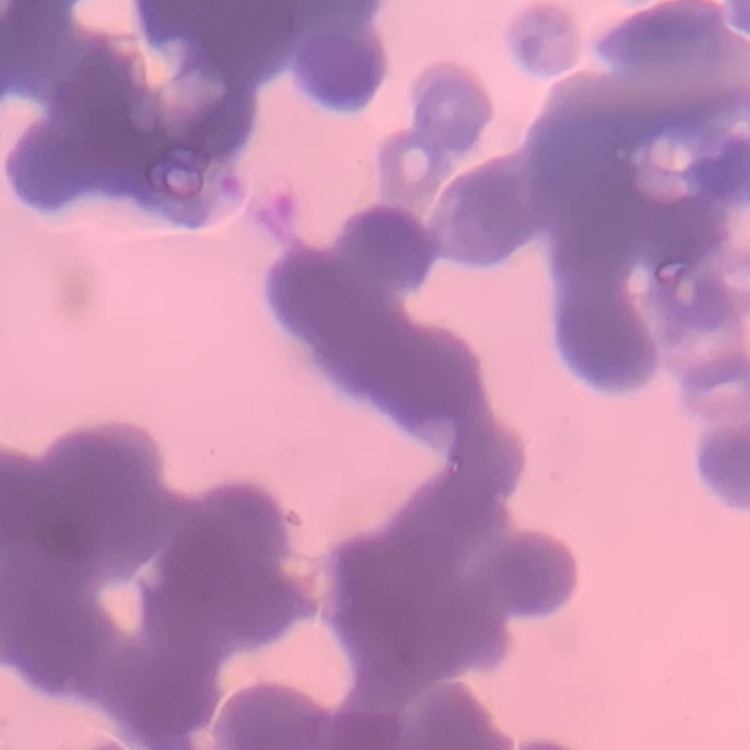
Summary:
  - Red blood cell morphology: rouleaux formation
  - Preparation: thin blood film
  - Image type: one tile cut from a larger photomicrograph
  - Stain: Field's or Giemsa